Give the location of every WBC.
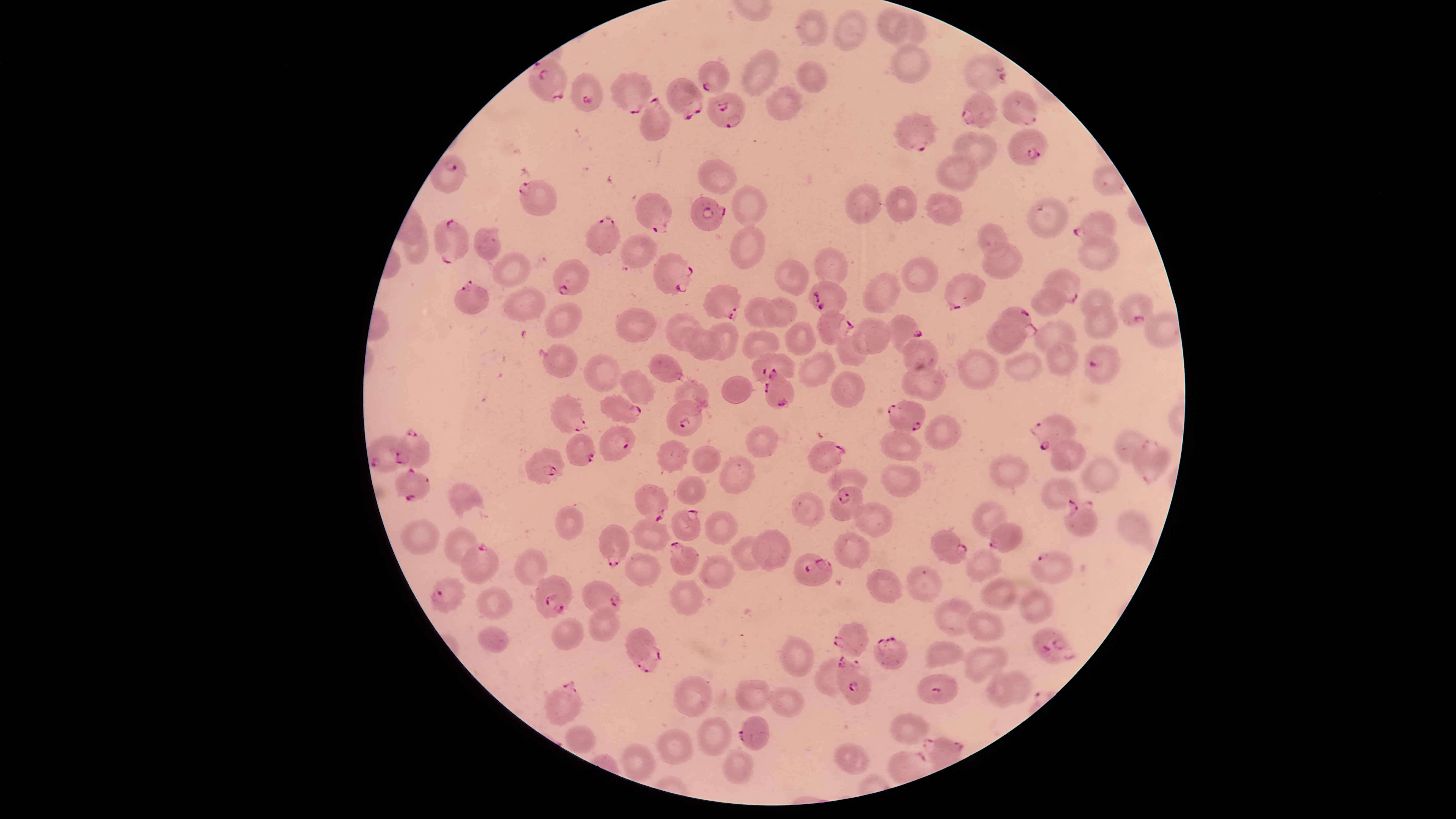
No WBCs identified.

Approximate bounding boxes as [left, top, right, bottom] in pixels.
Summary:
  - Parasitized RBCs: [964, 54, 1007, 93], [528, 57, 567, 102], [698, 61, 730, 94], [571, 72, 602, 112], [611, 72, 653, 114], [665, 78, 704, 121], [708, 90, 747, 128], [960, 90, 998, 129], [1002, 91, 1037, 126], [639, 96, 671, 141], [894, 112, 939, 153], [1007, 128, 1048, 165], [430, 155, 465, 194], [517, 180, 557, 215], [635, 192, 672, 233], [690, 198, 725, 230], [1072, 211, 1117, 251], [586, 214, 620, 255], [434, 218, 469, 264], [654, 253, 693, 295], [552, 259, 591, 295], [1040, 268, 1081, 303], [944, 272, 985, 311], [454, 278, 490, 314], [807, 281, 844, 316], [703, 284, 742, 321], [1119, 293, 1153, 325], [994, 307, 1037, 344], [817, 311, 855, 345], [885, 313, 923, 356], [1085, 344, 1122, 384], [752, 352, 793, 385], [763, 368, 793, 409], [550, 395, 588, 432], [599, 395, 640, 424], [666, 399, 703, 437], [887, 401, 925, 436], [1028, 414, 1077, 455], [394, 427, 429, 468], [599, 427, 635, 461], [566, 434, 595, 466], [366, 435, 413, 472], [1130, 439, 1171, 485], [807, 441, 846, 473], [525, 448, 566, 484], [394, 466, 431, 502], [634, 484, 669, 521], [830, 487, 863, 522], [1063, 499, 1098, 536], [670, 509, 701, 540], [987, 522, 1022, 554], [598, 524, 630, 568], [930, 530, 969, 565], [669, 540, 699, 575], [460, 542, 499, 584], [1030, 551, 1073, 583], [794, 553, 832, 586], [534, 574, 573, 619], [430, 576, 467, 613], [582, 580, 626, 619], [832, 621, 869, 656], [1033, 627, 1076, 664], [625, 629, 662, 673], [873, 636, 906, 668], [835, 654, 871, 707], [918, 674, 958, 703], [544, 679, 583, 726], [738, 716, 769, 750]
  - Uninfected RBCs: [874, 7, 908, 45], [833, 8, 867, 53], [796, 10, 828, 45], [892, 14, 926, 51], [890, 43, 932, 84], [741, 49, 780, 96], [796, 61, 828, 92], [765, 86, 802, 120], [951, 131, 998, 172], [935, 153, 978, 192], [698, 159, 737, 194], [845, 184, 881, 225], [731, 185, 766, 226], [884, 186, 916, 221], [923, 192, 964, 226], [1028, 198, 1069, 237], [978, 223, 1009, 259], [730, 224, 765, 269], [473, 227, 502, 259], [620, 235, 657, 268], [1078, 236, 1119, 272], [983, 243, 1023, 278], [814, 247, 848, 288], [492, 251, 531, 290], [900, 257, 938, 295], [774, 258, 809, 296], [864, 272, 900, 313], [503, 286, 546, 321], [1032, 287, 1065, 315], [1081, 289, 1113, 318], [744, 297, 780, 327], [762, 297, 797, 327], [546, 302, 584, 338], [1085, 305, 1118, 339], [615, 307, 656, 343], [1144, 312, 1180, 348], [665, 313, 705, 350], [853, 317, 891, 354], [987, 320, 1025, 356], [785, 321, 816, 355], [1034, 321, 1075, 354], [699, 323, 738, 360], [684, 329, 721, 360], [742, 329, 779, 360], [836, 335, 868, 366], [902, 339, 938, 376], [1045, 341, 1079, 376], [543, 345, 577, 378], [959, 348, 999, 390], [799, 351, 836, 386], [1004, 352, 1041, 380], [648, 354, 681, 383], [583, 355, 622, 391], [899, 366, 946, 401], [619, 370, 654, 405], [830, 372, 864, 407], [721, 376, 754, 403], [674, 380, 709, 417], [926, 415, 961, 450], [746, 425, 779, 458], [1114, 429, 1149, 464], [881, 431, 922, 460], [656, 440, 689, 474], [1051, 440, 1086, 472], [691, 445, 720, 474], [719, 456, 754, 493], [989, 456, 1030, 486], [1081, 458, 1119, 493], [881, 464, 922, 497], [677, 476, 707, 505], [1041, 478, 1077, 511], [448, 483, 484, 521], [792, 493, 825, 526], [852, 501, 893, 539], [972, 501, 1007, 539], [557, 506, 583, 539], [705, 511, 738, 544], [1118, 513, 1151, 542], [632, 517, 671, 550], [400, 519, 439, 556], [443, 527, 479, 566], [753, 529, 790, 572], [834, 533, 871, 568], [730, 535, 769, 570], [514, 548, 548, 587], [965, 548, 1002, 582], [626, 553, 660, 586], [698, 554, 734, 589], [906, 566, 943, 602], [867, 568, 902, 603], [979, 578, 1018, 611], [669, 580, 702, 616], [477, 587, 513, 619], [1020, 590, 1055, 625], [933, 599, 978, 636], [587, 607, 620, 642], [967, 611, 1006, 641], [551, 617, 583, 650], [477, 626, 509, 652], [781, 634, 816, 677], [926, 642, 967, 668], [963, 646, 1008, 683], [1000, 671, 1031, 703], [986, 673, 1016, 705], [673, 677, 712, 717], [736, 680, 773, 712], [767, 687, 804, 717], [888, 713, 929, 745], [698, 716, 732, 756], [563, 725, 597, 754], [657, 729, 693, 764], [622, 744, 655, 781], [833, 744, 869, 775], [722, 752, 754, 784]
  - Species: Plasmodium falciparum
  - Preparation: thin blood smear
  - Stain: Giemsa
  - Image size: 1456×819 pixels
  - Capture: smartphone photograph through the microscope eyepiece
  - Visible region: circular
  - Presence: malaria parasites identified
  - Field of view: single